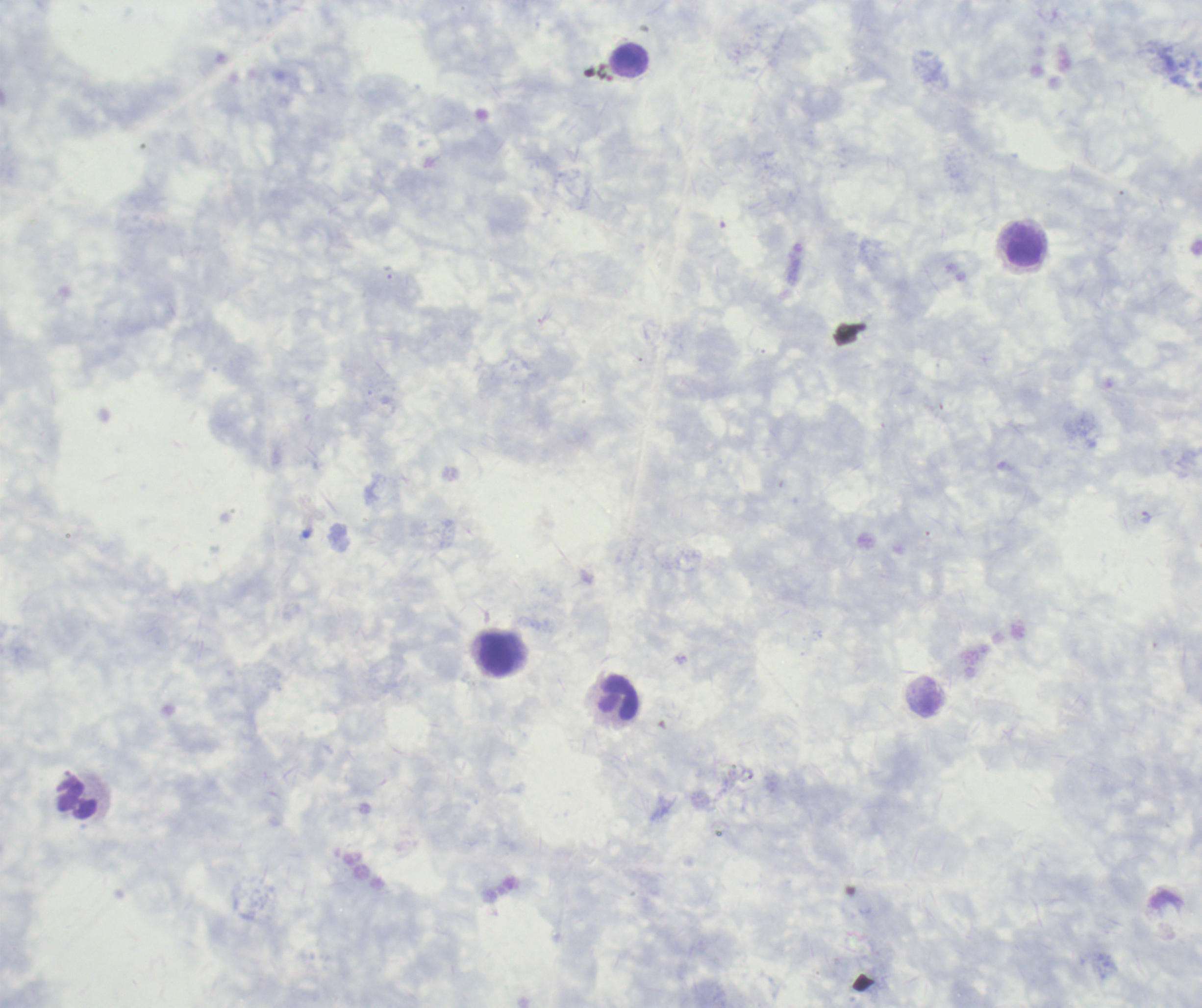
{
  "magnification": "100x",
  "context": "previously used in a real diagnosis",
  "field_of_view": "one from this slide",
  "result": "negative for malaria parasites",
  "image_size": "1202×1008 pixels",
  "preparation": "thick blood film",
  "leukocyte_locations": "approximate centers as (x, y) in pixels: (632, 60), (1025, 248), (499, 654), (619, 697), (76, 798)",
  "stain": "Romanowsky",
  "coloration_quality": "good",
  "background_quality": "poor"
}